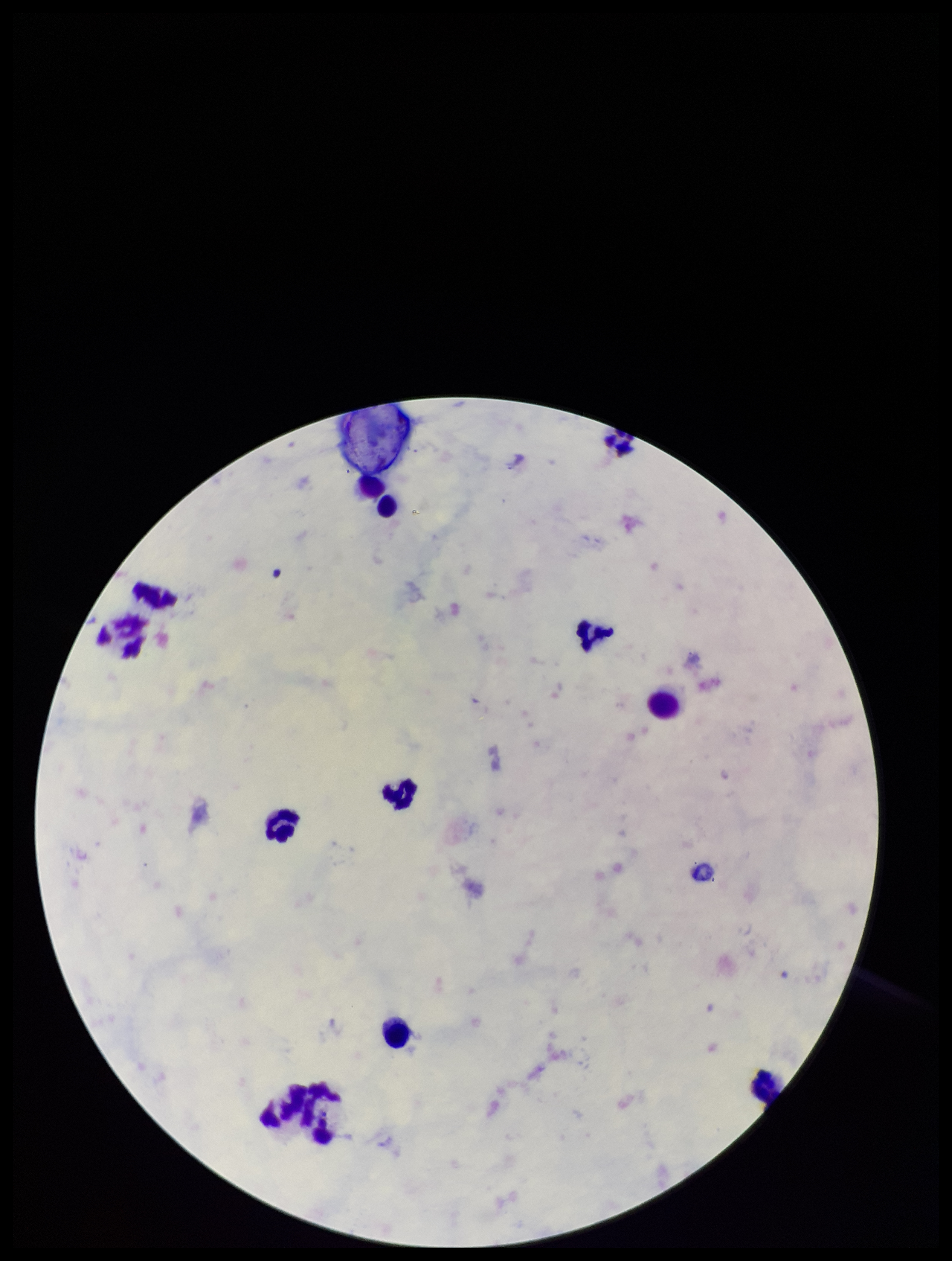
Summary:
  - Species reported for this patient: Plasmodium falciparum
  - Field of view: single
  - Image size: 952×1261 pixels
  - Preparation: thick
  - Plasmodium parasites: none seen
  - Parasite count: 0
  - Stain: Giemsa
  - Leukocyte count: 13
  - Capture: smartphone photograph through the microscope eyepiece
  - Patient malaria status: infected